Name the parasite shown.
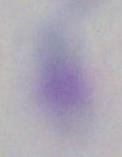

Toxoplasma gondii.

Summary:
  - Magnification: 1000x
  - Modality: photomicrograph